Report the malaria status of this cell.
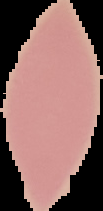

Uninfected.

image size = 103×211 pixels
preparation = thin blood smear
image type = segmented cell region on a black background